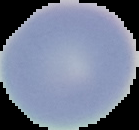

Image is 139×130 pixels. From a thin blood smear. Segmented cell region on a black background. Result: negative for malaria parasites.